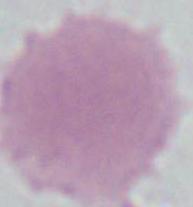

Summary:
  - Modality: photomicrograph
  - Magnification: 1000x
  - Identification: erythrocyte